Locate every malaria parasite.
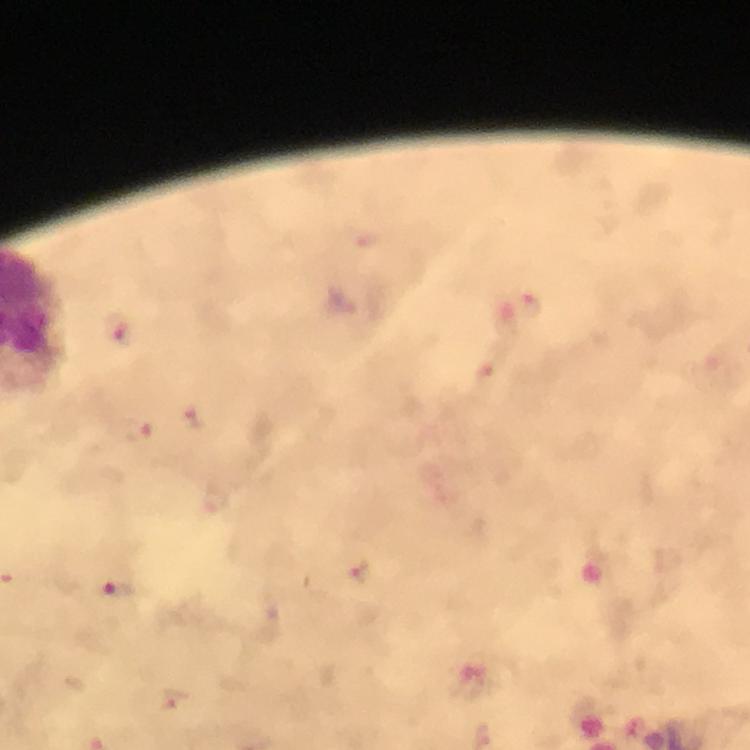
Approximate centers as {x, y} in pixels.
Malaria parasites: {530, 305}, {121, 331}, {191, 419}, {139, 431}, {358, 571}, {118, 591}.

{
  "capture": "smartphone photograph through a microscope",
  "immersion_oil": "used",
  "cropped_from": "one field of view",
  "preparation": "thick smear",
  "stain": "Giemsa",
  "context": "from a diagnostic examination for malaria",
  "image_size": "750×750 pixels",
  "magnification": "100x"
}